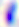

Summary:
  - Modality: micrograph
  - Magnification: 400x
  - Identification: Toxoplasma gondii